State which cell type is depicted.
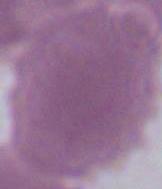
An erythrocyte.

{
  "modality": "micrograph",
  "magnification": "1000x"
}